Locate every Plasmodium parasite.
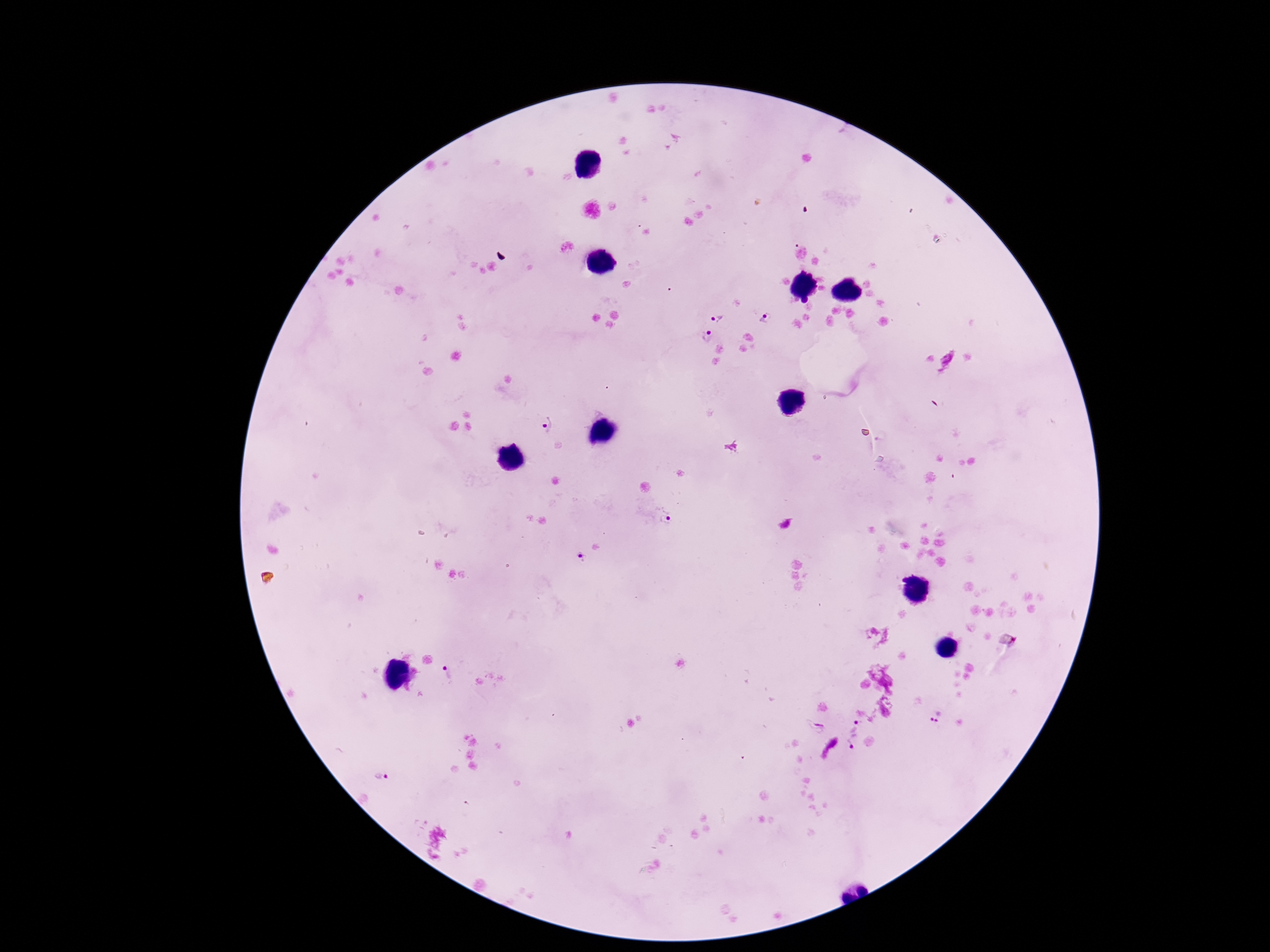
Approximate centers as [x, y] in pixels.
Plasmodium parasites: [765, 318], [717, 319], [707, 335], [547, 426], [666, 516], [579, 559], [446, 674], [937, 715], [853, 725], [817, 728], [853, 742], [378, 777].

Thick blood smear. Photographed through the microscope eyepiece with a smartphone camera. Single field of view. Giemsa-stained preparation. 100x magnification. Image is 1270×952 pixels. Patient malaria status: positive.